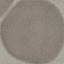
Malaria status: uninfected. Automatically extracted cell patch, resized to 64 × 64 pixels. Thin blood smear. Giemsa stain. Photographed with a smartphone camera at the microscope eyepiece.